Assess this cell for malaria.
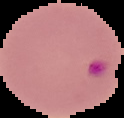
Parasitized.

From a thin blood film. Image is 124×118 pixels. Segmented cell region on a black background.